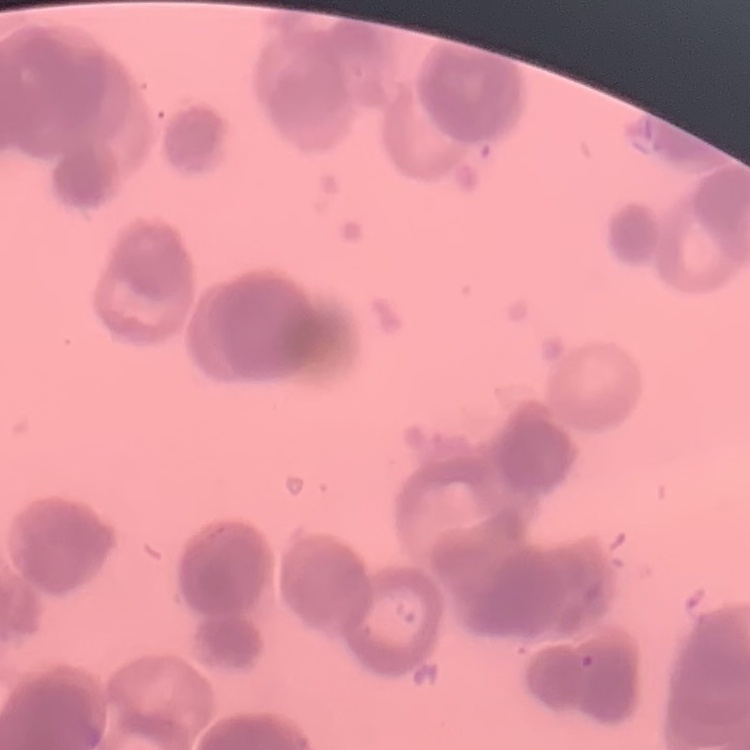
Summary:
  - Red blood cell morphology: rouleaux formation
  - Stain: Field's or Giemsa
  - Preparation: thin peripheral smear
  - Image type: one tile cut from a larger photomicrograph